State which parasite is depicted.
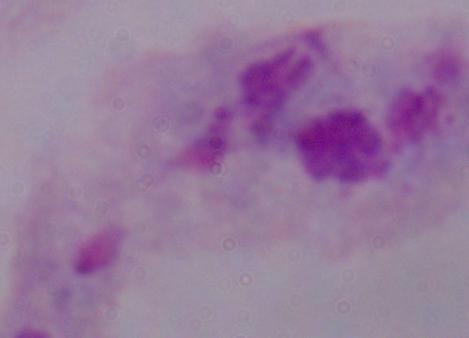
This is a trichomonad.

magnification = 1000x
modality = photomicrograph